Locate and identify every blood parasite.
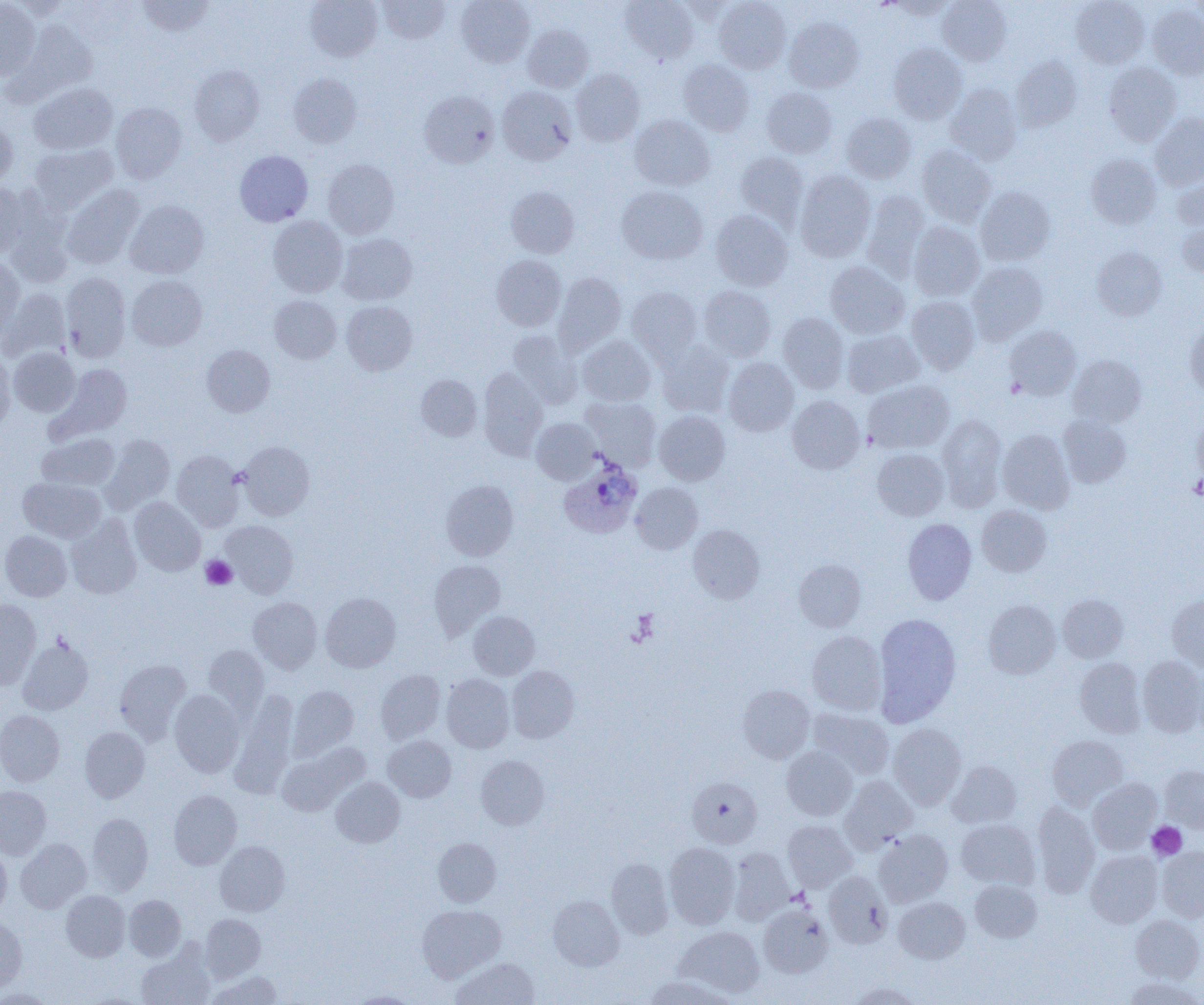
Approximate bounding boxes as [x1, y1, x2, y2] in pixels.
Plasmodium ovale-infected red blood cells: [559, 460, 642, 538].
No Plasmodium falciparum, Plasmodium malariae, Plasmodium vivax, Babesia divergens, or Trypanosoma brucei observed.

Summary:
  - Platelet locations: [1189, 473, 1204, 499], [201, 555, 237, 589], [1146, 821, 1187, 860]
  - Uninfected red blood cell locations: [8, 0, 73, 20], [136, 0, 214, 36], [305, 0, 382, 62], [378, 0, 449, 43], [456, 0, 535, 67], [621, 0, 699, 64], [678, 0, 746, 24], [714, 0, 791, 73], [885, 0, 959, 19], [938, 0, 1011, 66], [1071, 0, 1149, 68], [1188, 0, 1204, 22], [0, 1, 41, 80], [1147, 3, 1204, 79], [784, 17, 863, 92], [9, 22, 97, 104], [522, 25, 593, 92], [889, 44, 966, 123], [1011, 56, 1082, 132], [679, 60, 754, 136], [1104, 62, 1182, 145], [189, 65, 265, 144], [571, 69, 644, 146], [288, 73, 362, 148], [29, 83, 118, 154], [945, 84, 1022, 164], [497, 86, 577, 165], [761, 87, 837, 158], [419, 90, 499, 168], [111, 103, 187, 183], [841, 112, 915, 183], [1150, 113, 1204, 189], [630, 115, 715, 190], [0, 120, 17, 188], [29, 144, 116, 212], [917, 144, 995, 227], [235, 150, 313, 226], [735, 151, 808, 228], [1086, 154, 1161, 229], [322, 158, 399, 239], [1172, 167, 1204, 231], [795, 170, 875, 262], [0, 184, 28, 259], [62, 184, 144, 269], [506, 186, 579, 258], [616, 186, 707, 264], [975, 186, 1055, 266], [862, 190, 930, 280], [125, 200, 209, 279], [4, 204, 73, 287], [711, 210, 793, 291], [268, 216, 348, 297], [1177, 220, 1204, 278], [908, 222, 984, 300], [337, 233, 417, 305], [1092, 246, 1167, 321], [491, 255, 566, 330], [0, 257, 25, 339], [825, 261, 909, 338], [967, 262, 1047, 344], [60, 272, 131, 362], [554, 272, 626, 354], [126, 275, 206, 351], [699, 285, 776, 361], [627, 286, 701, 364], [2, 289, 70, 362], [269, 295, 341, 363], [906, 296, 980, 374], [341, 301, 417, 375], [778, 313, 849, 393], [1184, 321, 1204, 398], [1004, 325, 1081, 400], [507, 330, 582, 408], [842, 330, 924, 397], [576, 335, 656, 406], [658, 342, 734, 417], [202, 345, 275, 416], [9, 347, 80, 416], [0, 350, 14, 433], [1068, 355, 1146, 427], [724, 358, 799, 436], [53, 363, 132, 440], [479, 368, 548, 460], [416, 374, 482, 441], [863, 379, 954, 454], [787, 395, 863, 473], [580, 396, 661, 471], [654, 411, 730, 485], [937, 415, 1007, 510], [1058, 415, 1131, 487], [1193, 415, 1204, 483], [531, 418, 600, 484], [997, 429, 1075, 513], [37, 433, 119, 491], [100, 434, 175, 512], [239, 441, 314, 520], [872, 449, 949, 521], [172, 450, 244, 532], [19, 477, 106, 542], [440, 480, 518, 561], [630, 483, 703, 554], [129, 497, 205, 576], [977, 505, 1052, 576], [66, 515, 142, 599], [903, 518, 976, 604], [221, 520, 298, 597], [688, 524, 764, 603], [0, 530, 71, 601], [794, 559, 866, 631], [429, 560, 505, 639], [320, 593, 401, 672], [1057, 593, 1128, 662], [1167, 595, 1204, 672], [248, 596, 322, 673], [0, 598, 41, 689], [983, 600, 1060, 679], [469, 611, 539, 679], [873, 613, 961, 726], [807, 631, 886, 715], [18, 637, 93, 715], [203, 644, 270, 717], [1138, 656, 1204, 737], [1075, 658, 1147, 737], [114, 659, 190, 741], [507, 666, 579, 743], [376, 670, 446, 744], [441, 674, 514, 752], [738, 684, 815, 763], [288, 685, 358, 759], [170, 689, 244, 777], [230, 690, 298, 795], [809, 708, 894, 779], [0, 710, 65, 786], [888, 723, 967, 809], [80, 727, 149, 802], [383, 735, 456, 802], [1047, 735, 1129, 809], [782, 746, 857, 820], [277, 747, 360, 815], [476, 755, 549, 829], [946, 760, 1021, 828], [1160, 765, 1204, 832], [687, 776, 762, 848], [839, 776, 918, 852], [331, 777, 405, 847], [1088, 779, 1162, 853], [0, 786, 51, 859], [169, 790, 241, 869], [1033, 802, 1100, 897], [86, 813, 153, 895], [956, 819, 1040, 890], [783, 820, 857, 891], [874, 829, 953, 907], [15, 838, 91, 913], [433, 838, 501, 906], [214, 841, 289, 915], [664, 842, 740, 928], [0, 846, 11, 920], [1157, 847, 1204, 922], [729, 848, 794, 924], [1085, 850, 1162, 927], [607, 858, 673, 939], [824, 871, 892, 948], [970, 880, 1042, 942], [61, 890, 130, 961], [124, 895, 186, 961], [549, 896, 624, 970], [893, 897, 969, 963], [417, 904, 505, 982], [758, 904, 833, 977], [0, 914, 26, 993], [200, 914, 265, 982], [1131, 914, 1204, 983], [675, 926, 764, 997], [136, 943, 215, 1005], [452, 958, 539, 1005], [205, 971, 283, 1005], [644, 975, 735, 1005], [1123, 977, 1203, 1005], [849, 982, 921, 1005], [1, 988, 52, 1004], [350, 992, 419, 1005]
  - Slide-level diagnosis: Plasmodium ovale
  - Image size: 1204×1005 pixels
  - Modality: optical microscopy
  - Field of view: single
  - Preparation: thin blood smear
  - Magnification: 1000x